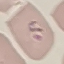

Summary:
  - Malaria status: parasitized
  - Capture: smartphone camera at the microscope eyepiece
  - Preparation: thin smear
  - Image type: cell patch, automatically extracted from a larger field of view and resized to 64 × 64 pixels
  - Stain: Giemsa